Outline each blood parasite and name the species.
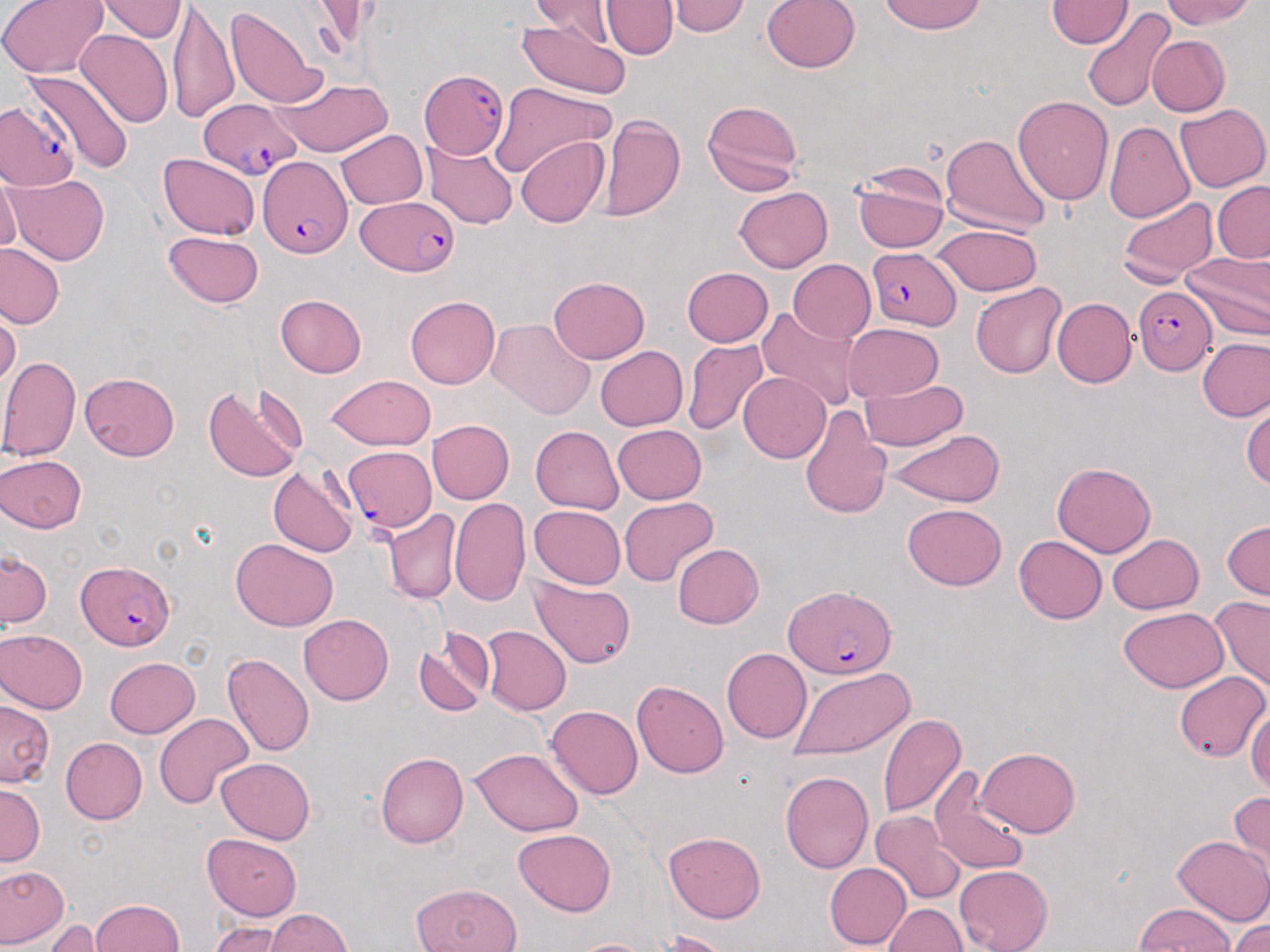

Approximate bounding boxes as [x1, y1, x2, y2] in pixels.
Plasmodium falciparum-infected red blood cells: [418, 71, 510, 159], [199, 98, 303, 179], [0, 99, 77, 192], [260, 158, 354, 258], [355, 195, 461, 278], [867, 249, 959, 330], [1134, 287, 1216, 375], [341, 446, 436, 533], [78, 561, 175, 651], [780, 584, 899, 679].
No Plasmodium ovale, Plasmodium malariae, Plasmodium vivax, Babesia divergens, or Trypanosoma brucei observed.

Summary:
  - Uninfected red blood cell locations: [1, 0, 108, 76], [672, 0, 748, 37], [760, 0, 861, 74], [878, 0, 987, 35], [1162, 0, 1257, 32], [101, 1, 184, 43], [527, 1, 615, 46], [603, 1, 673, 59], [169, 2, 239, 120], [1046, 2, 1131, 49], [227, 6, 325, 108], [1082, 10, 1177, 112], [515, 18, 631, 100], [76, 28, 173, 125], [1145, 35, 1229, 116], [23, 68, 135, 174], [275, 78, 391, 155], [490, 82, 618, 179], [1014, 95, 1116, 205], [700, 100, 803, 197], [1176, 103, 1269, 192], [599, 112, 687, 225], [1105, 119, 1195, 225], [336, 128, 429, 210], [938, 133, 1052, 234], [516, 135, 610, 227], [425, 137, 518, 228], [158, 153, 260, 239], [851, 163, 952, 254], [7, 172, 106, 264], [1, 175, 20, 259], [1212, 182, 1270, 262], [735, 188, 833, 273], [1119, 192, 1217, 283], [930, 225, 1043, 296], [161, 229, 266, 308], [1, 244, 66, 329], [1183, 253, 1269, 342], [787, 259, 876, 344], [681, 267, 774, 347], [547, 277, 651, 367], [971, 283, 1066, 378], [276, 295, 367, 377], [405, 296, 499, 390], [1052, 298, 1136, 387], [755, 307, 864, 410], [2, 311, 19, 390], [485, 318, 595, 420], [842, 324, 944, 403], [683, 337, 769, 435], [1198, 338, 1270, 422], [594, 345, 688, 431], [0, 355, 80, 464], [80, 371, 182, 460], [738, 372, 832, 462], [325, 376, 438, 452], [858, 376, 970, 451], [201, 383, 307, 486], [1243, 404, 1270, 496], [799, 407, 893, 520], [426, 418, 513, 505], [613, 423, 708, 502], [531, 426, 624, 515], [886, 428, 1005, 505], [0, 453, 89, 531], [1053, 461, 1155, 556], [268, 465, 357, 557], [450, 495, 532, 608], [621, 496, 718, 586], [902, 503, 1007, 590], [529, 505, 626, 589], [382, 507, 458, 604], [1220, 520, 1269, 599], [1013, 534, 1106, 624], [1108, 535, 1203, 614], [230, 539, 339, 631], [673, 543, 764, 629], [1, 549, 52, 631], [529, 577, 637, 668], [1206, 597, 1270, 692], [1118, 608, 1229, 692], [298, 614, 393, 705], [481, 626, 571, 714], [0, 630, 88, 713], [414, 636, 491, 718], [722, 647, 811, 743], [222, 652, 314, 758], [105, 654, 200, 736], [788, 667, 917, 756], [1173, 673, 1268, 764], [632, 680, 730, 777], [0, 700, 57, 788], [1248, 703, 1270, 801], [548, 706, 641, 799], [877, 711, 966, 820], [154, 713, 254, 809], [59, 737, 146, 824], [976, 747, 1079, 836], [469, 749, 585, 837], [374, 751, 467, 849], [216, 757, 314, 844], [928, 766, 1031, 878], [780, 769, 874, 872], [0, 785, 44, 863], [1227, 789, 1269, 869], [870, 809, 962, 904], [514, 826, 615, 913], [665, 831, 768, 923], [203, 832, 305, 919], [1171, 833, 1270, 925], [830, 836, 955, 944], [823, 862, 909, 949], [0, 864, 67, 945], [954, 865, 1054, 952], [408, 881, 524, 952], [27, 894, 101, 943], [88, 898, 188, 952], [885, 903, 970, 952], [1130, 905, 1237, 951], [263, 909, 356, 952], [1227, 911, 1270, 952], [49, 917, 99, 950], [203, 919, 292, 950], [657, 929, 730, 952], [565, 935, 663, 952]
  - Slide-level diagnosis: Plasmodium falciparum
  - Preparation: thin blood film
  - Magnification: 1000x
  - Stain: May-Grünwald-Giemsa
  - Modality: optical microscopy
  - Field of view: one of a larger specimen
  - Image size: 1270×952 pixels